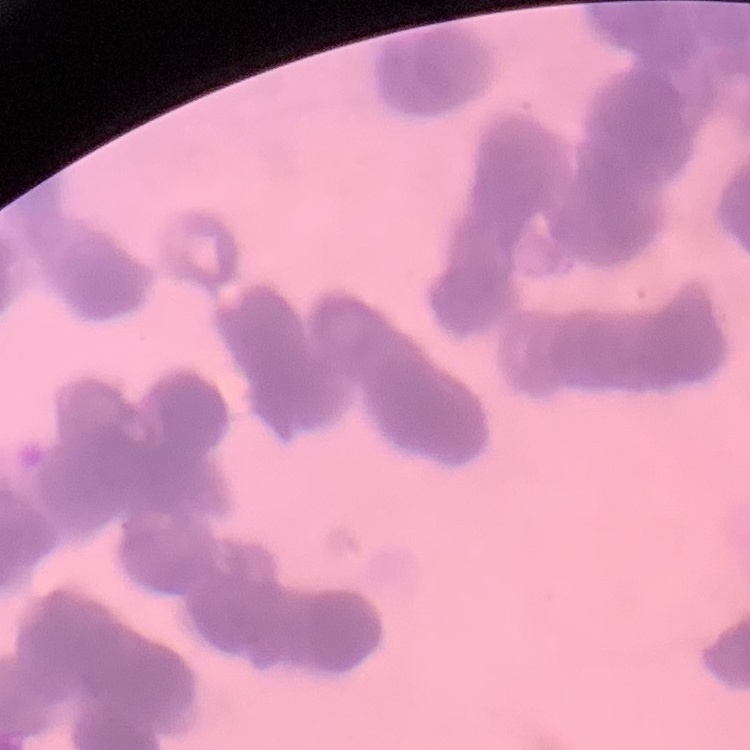
The erythrocytes exhibit rouleaux formation. One tile cut from a larger photomicrograph. Field's or Giemsa stain. Thin peripheral smear.